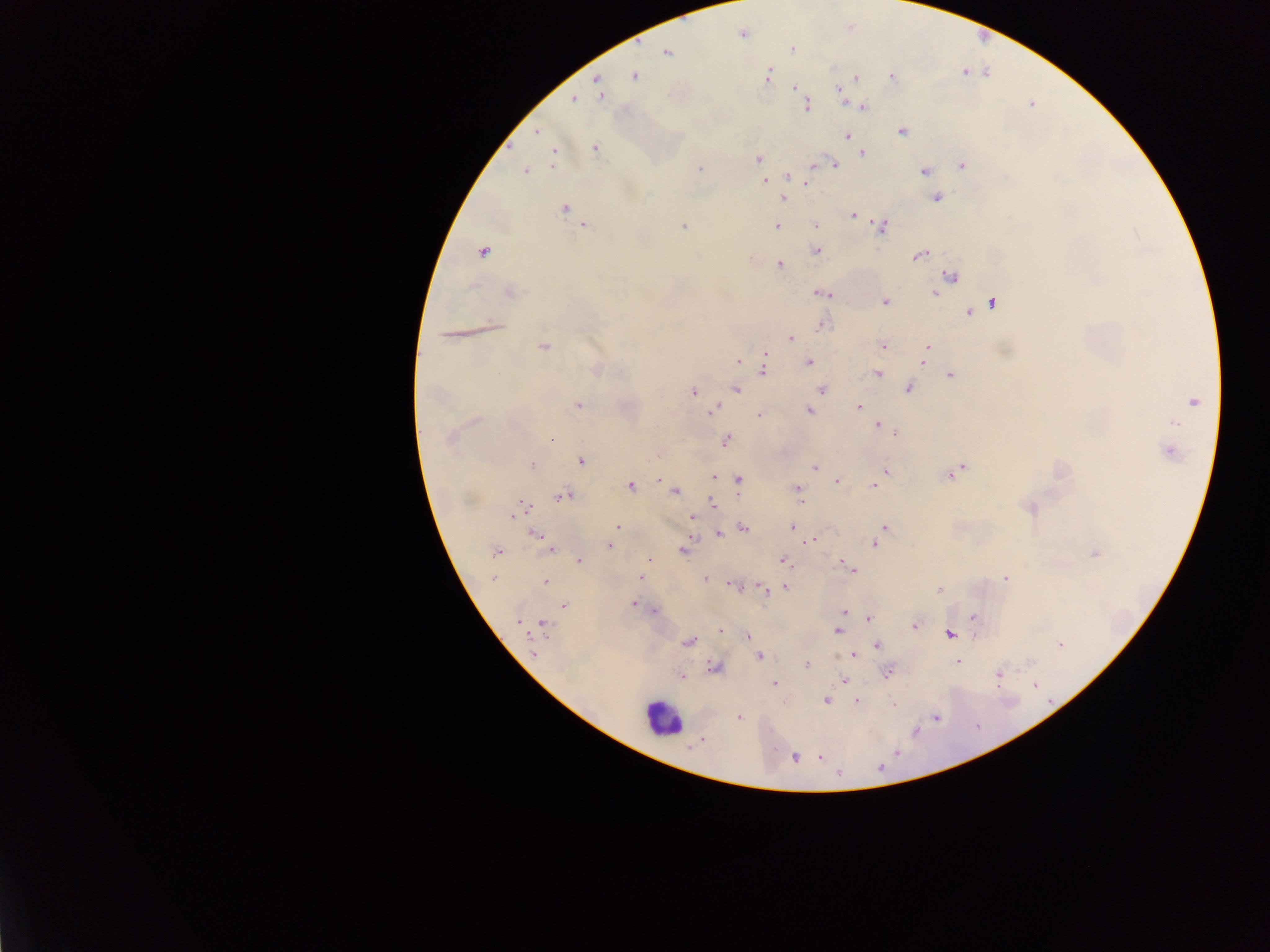
country = Ghana
preparation = thick blood film
image size = 1270×952 pixels
capture = mobile-phone photograph through a microscope
field of view = single
Plasmodium parasite locations = approximate centers as {x, y} in pixels: {742, 34}, {792, 49}, {667, 52}, {634, 76}, {768, 76}, {892, 78}, {855, 79}, {597, 80}, {795, 87}, {839, 91}, {601, 95}, {574, 99}, {807, 106}, {862, 107}, {538, 131}, {902, 131}, {847, 135}, {594, 147}, {862, 153}, {553, 155}, {758, 158}, {815, 164}, {834, 164}, {962, 165}, {700, 168}, {525, 171}, {925, 171}, {788, 177}, {764, 182}, {806, 183}, {937, 197}, {783, 198}, {564, 208}, {853, 214}, {815, 224}, {585, 226}, {777, 226}, {881, 226}, {683, 227}, {816, 250}, {482, 253}, {918, 255}, {779, 265}, {951, 276}, {511, 292}, {822, 293}, {935, 293}, {885, 302}, {992, 303}, {970, 313}, {822, 326}, {790, 339}, {544, 347}, {883, 347}, {927, 349}, {924, 358}, {738, 361}, {809, 362}, {763, 368}, {597, 369}, {878, 373}, {950, 375}, {909, 388}, {735, 389}, {822, 389}, {694, 392}, {1194, 401}, {578, 406}, {859, 406}, {714, 411}, {808, 411}, {760, 415}, {476, 420}, {1173, 422}, {878, 426}, {894, 432}, {551, 438}, {449, 439}, {727, 441}, {1169, 452}, {582, 461}, {532, 465}, {963, 467}, {815, 468}, {886, 471}, {950, 475}, {713, 477}, {738, 480}, {660, 481}, {838, 481}, {630, 486}, {874, 486}, {797, 488}, {675, 491}, {563, 496}, {712, 503}, {1030, 508}, {518, 511}, {691, 517}, {792, 526}, {617, 527}, {885, 527}, {743, 528}, {718, 533}, {535, 534}, {881, 536}, {812, 540}, {875, 545}, {609, 546}, {683, 549}, {551, 550}, {496, 551}, {1094, 554}, {649, 560}, {784, 560}, {579, 561}, {850, 568}, {640, 577}, {493, 578}, {1005, 578}, {705, 579}, {545, 581}, {732, 585}, {785, 587}, {764, 588}, {940, 589}, {633, 604}, {564, 605}, {653, 611}, {844, 611}, {974, 617}, {869, 618}, {517, 620}, {544, 625}, {914, 626}, {720, 631}, {837, 631}, {950, 635}, {748, 636}, {688, 642}, {1061, 643}, {877, 645}, {533, 650}, {853, 655}, {760, 657}, {957, 662}, {807, 665}, {714, 667}, {888, 673}, {999, 674}, {682, 676}, {843, 680}, {774, 683}, {1034, 685}, {826, 700}, {857, 701}, {894, 705}, {739, 717}, {820, 757}, {794, 758}
leukocyte locations = approximate centers as {x, y} in pixels: {662, 719}